Locate every leukocyte (white blood cell).
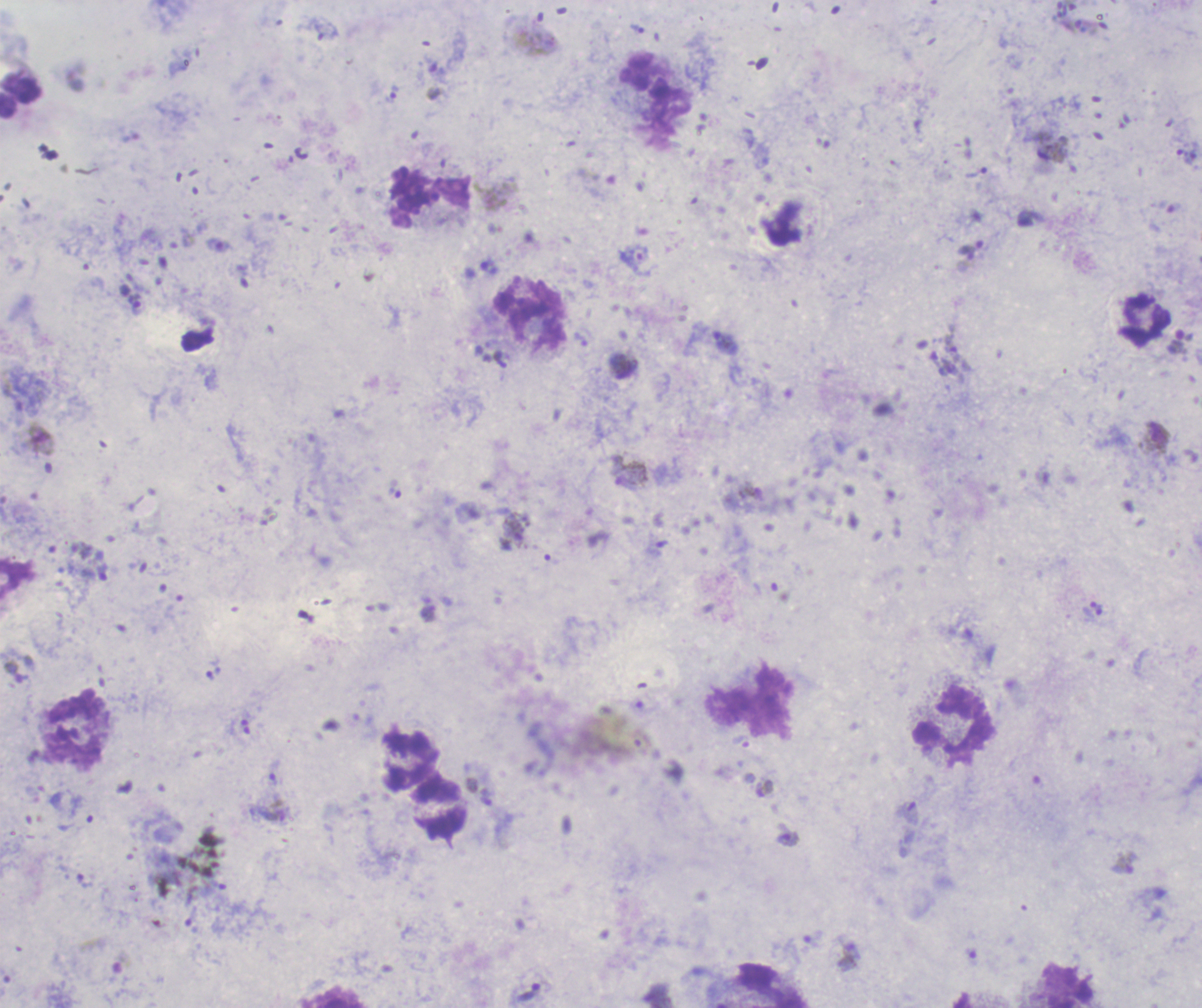
Approximate object centers, in pixels from the top-left corner.
Leukocytes: (x=20, y=96), (x=429, y=197), (x=1145, y=321), (x=953, y=725), (x=76, y=731), (x=409, y=758), (x=440, y=808), (x=774, y=984), (x=1065, y=986).

Approximate object centers, in pixels from the top-left corner. Trophozoite locations: (x=975, y=173), (x=634, y=257), (x=137, y=304), (x=726, y=343), (x=513, y=531), (x=14, y=672), (x=787, y=839), (x=528, y=991). Gametocyte locations: (x=1156, y=437), (x=41, y=440), (x=632, y=474), (x=765, y=789), (x=1124, y=864). Life-cycle stages observed: trophozoite, gametocyte. 100x magnification. Image is 1202×1008 pixels. One field from this slide. Thick blood smear. Result: malaria parasites detected. Romanowsky stain. Previously used in a real diagnosis. Background quality: good.